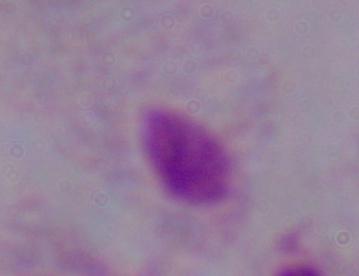
identification = trichomonad
magnification = 1000x
modality = photomicrograph